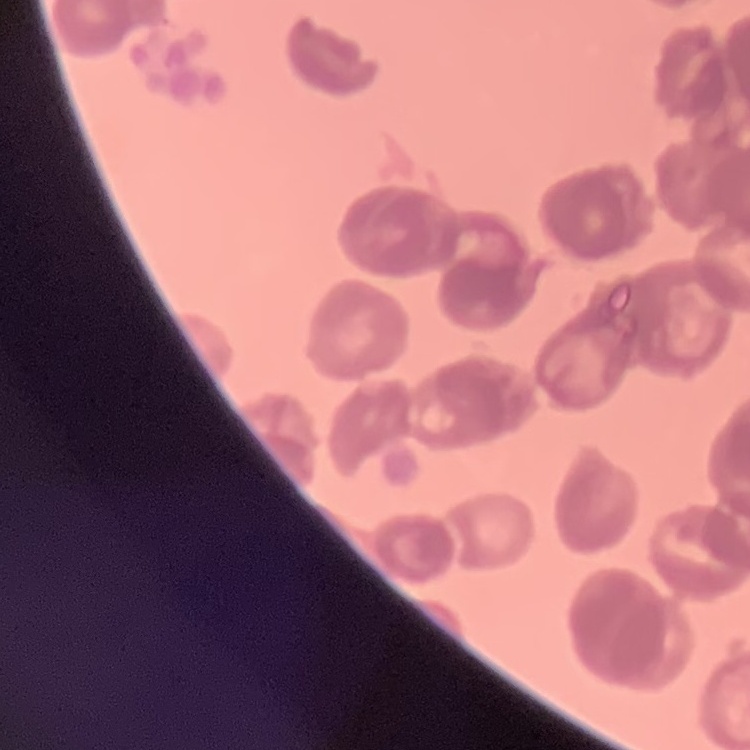
The red blood cells exhibit rouleaux formation. Thin peripheral smear. Square crop of a larger photomicrograph. Field's or Giemsa stain.